Report the malaria status of this cell.
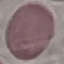
Uninfected.

Acquired by smartphone through the microscope eyepiece. Automatically extracted cell patch, resized to 64 × 64 pixels. Thin smear of blood. Giemsa stain.